Classify this cell by malaria status.
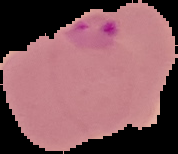

Parasitized.

Summary:
  - Image size: 178×154 pixels
  - Image type: cell region segmented out of the field of view; surrounding area masked to black
  - Preparation: thin blood film